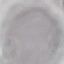
{
  "malaria_status": "uninfected",
  "preparation": "thin blood film",
  "image_type": "cell patch, automatically extracted from a larger field of view and resized to 64 × 64 pixels",
  "capture": "smartphone camera at the microscope eyepiece",
  "stain": "Giemsa"
}